Give the preparation type.
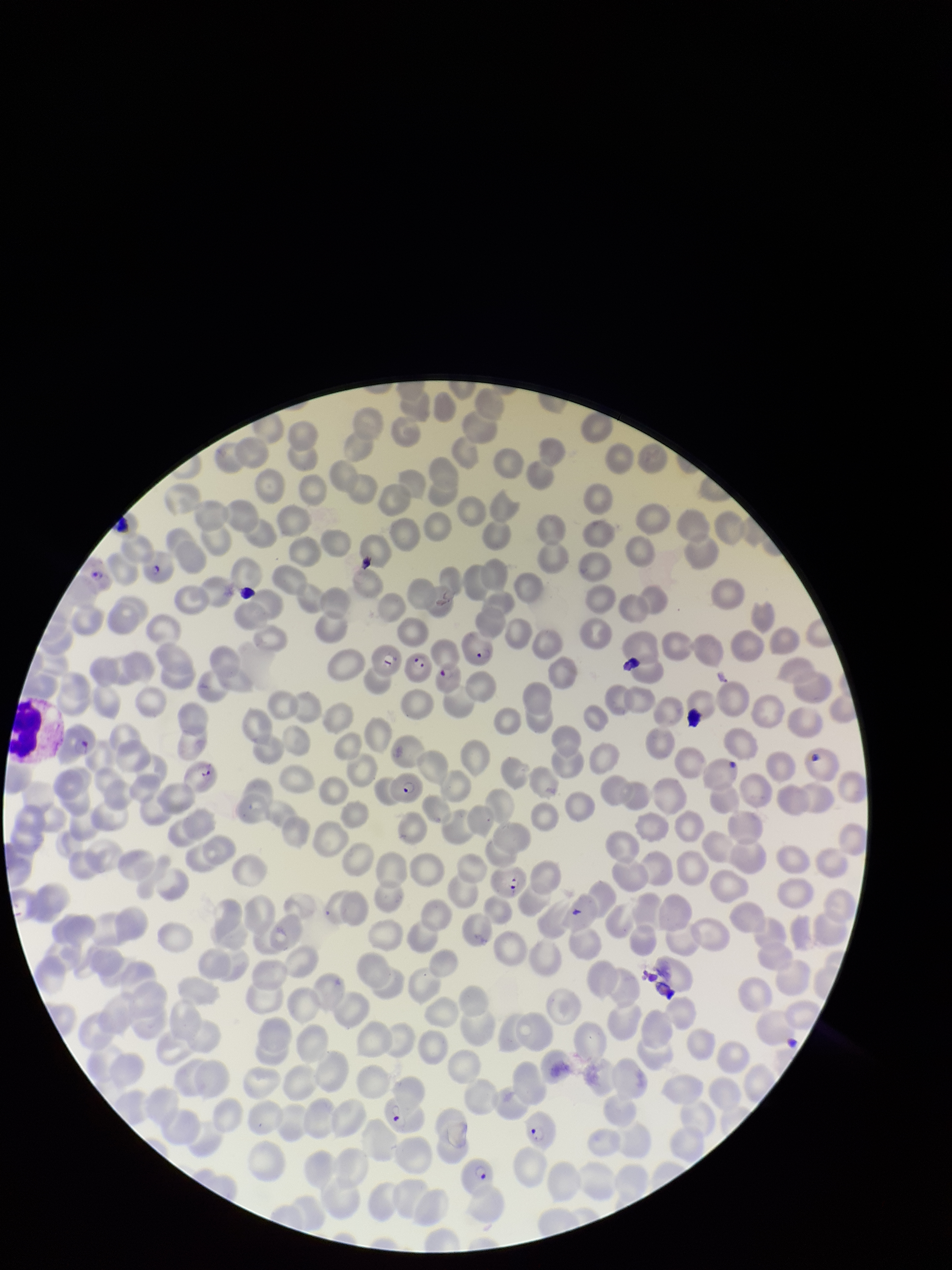

Thin.

Summary:
  - Image size: 952×1270 pixels
  - Field of view: one from this slide
  - Stain: Giemsa
  - Parasitized red blood cells: seen
  - Patient malaria status: positive
  - Capture: smartphone photograph through the microscope eyepiece
  - Red blood cell count: 235
  - Parasitized red blood cell count: 13
  - Species reported for this patient: Plasmodium falciparum